Assess the morphology of the erythrocytes.
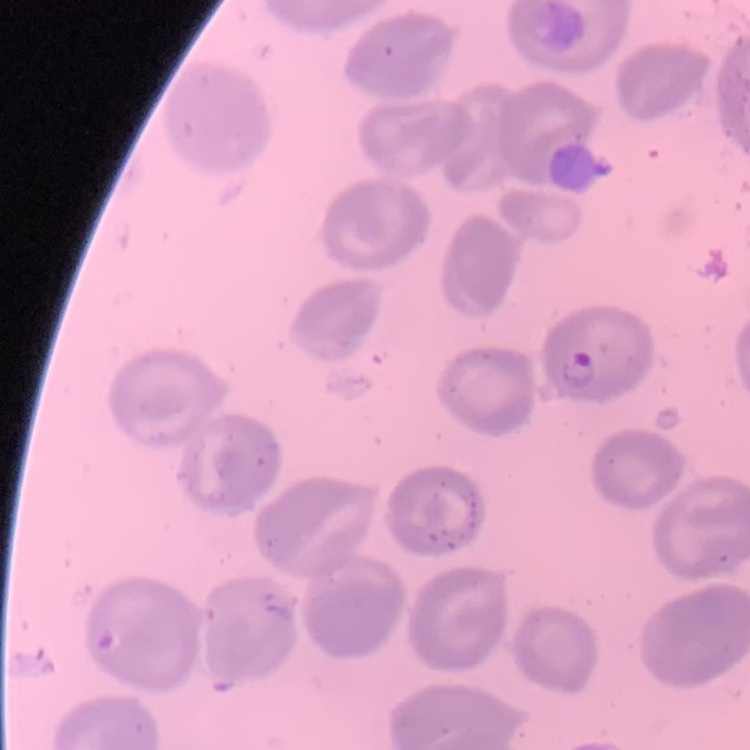

They show no rouleaux formation.

Field's or Giemsa stain. Square crop of a larger photomicrograph. Thin blood film.